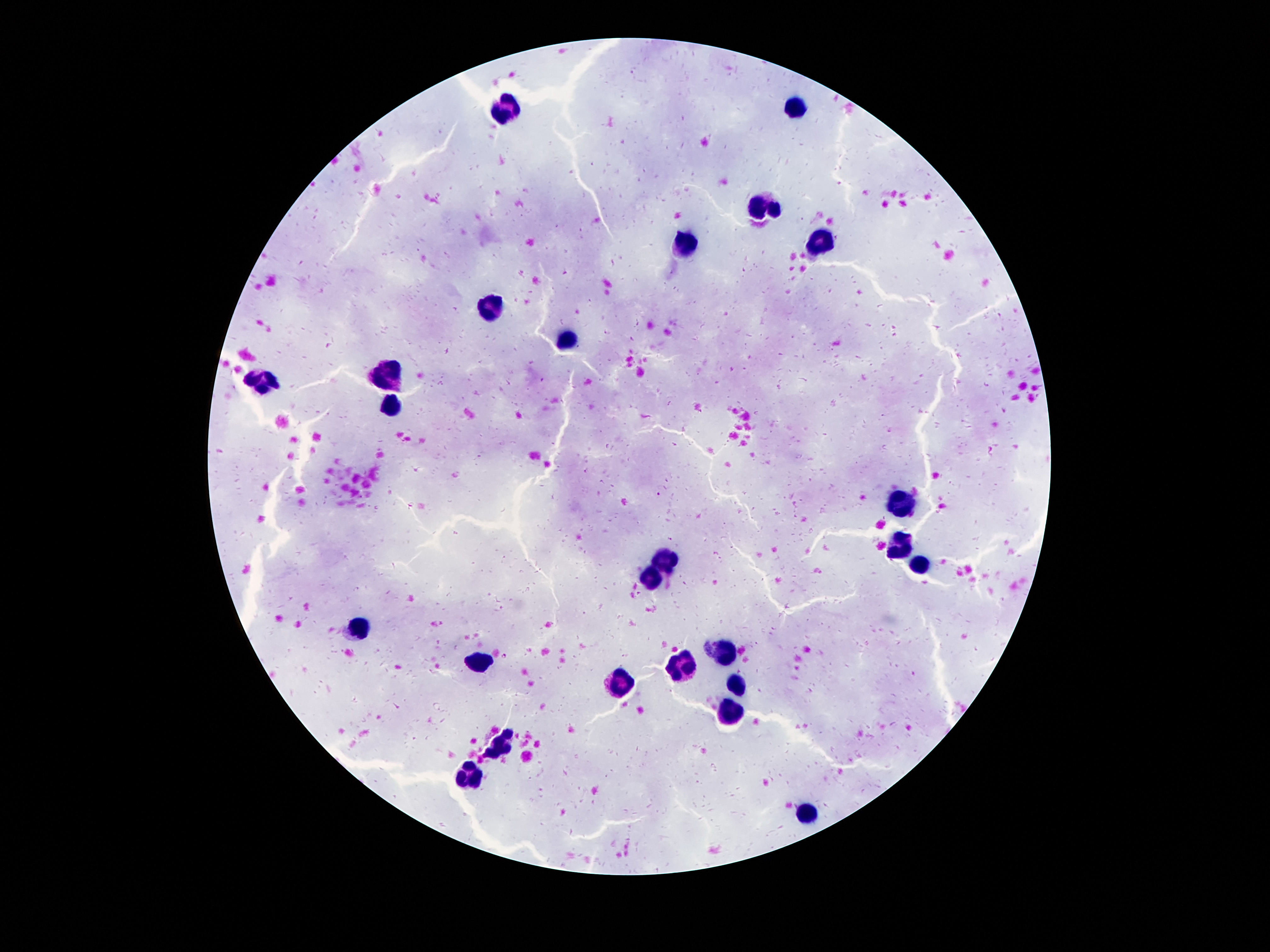 Approximate centers as (x, y) in pixels. Leukocyte locations: (796, 108), (501, 109), (764, 208), (820, 238), (686, 246), (488, 307), (563, 340), (389, 378), (264, 383), (395, 406), (904, 501), (900, 546), (667, 559), (919, 565), (647, 577), (358, 630), (721, 650), (481, 663), (682, 667), (619, 682), (736, 686), (729, 708), (499, 744), (468, 775), (809, 811). Photographed through the microscope eyepiece with a smartphone camera. Giemsa-stained preparation. 100x magnification. Thick blood smear. Image is 1270×952 pixels. One field from this slide. Patient malaria status: uninfected.